Identify the parasite.
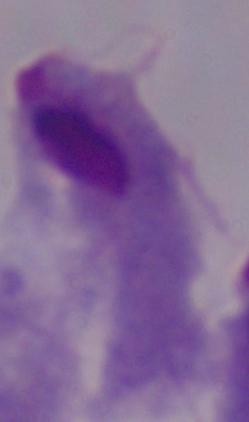
A trichomonad.

Summary:
  - Magnification: 1000x
  - Modality: photomicrograph